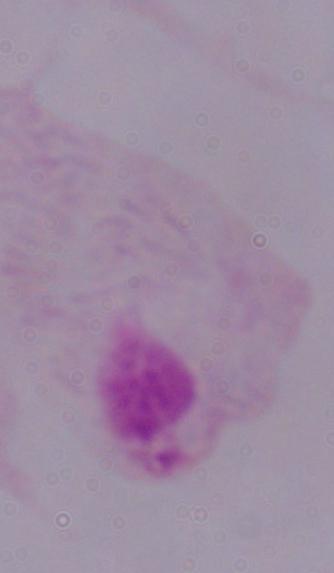

{
  "modality": "photomicrograph",
  "magnification": "1000x",
  "identification": "trichomonad"
}